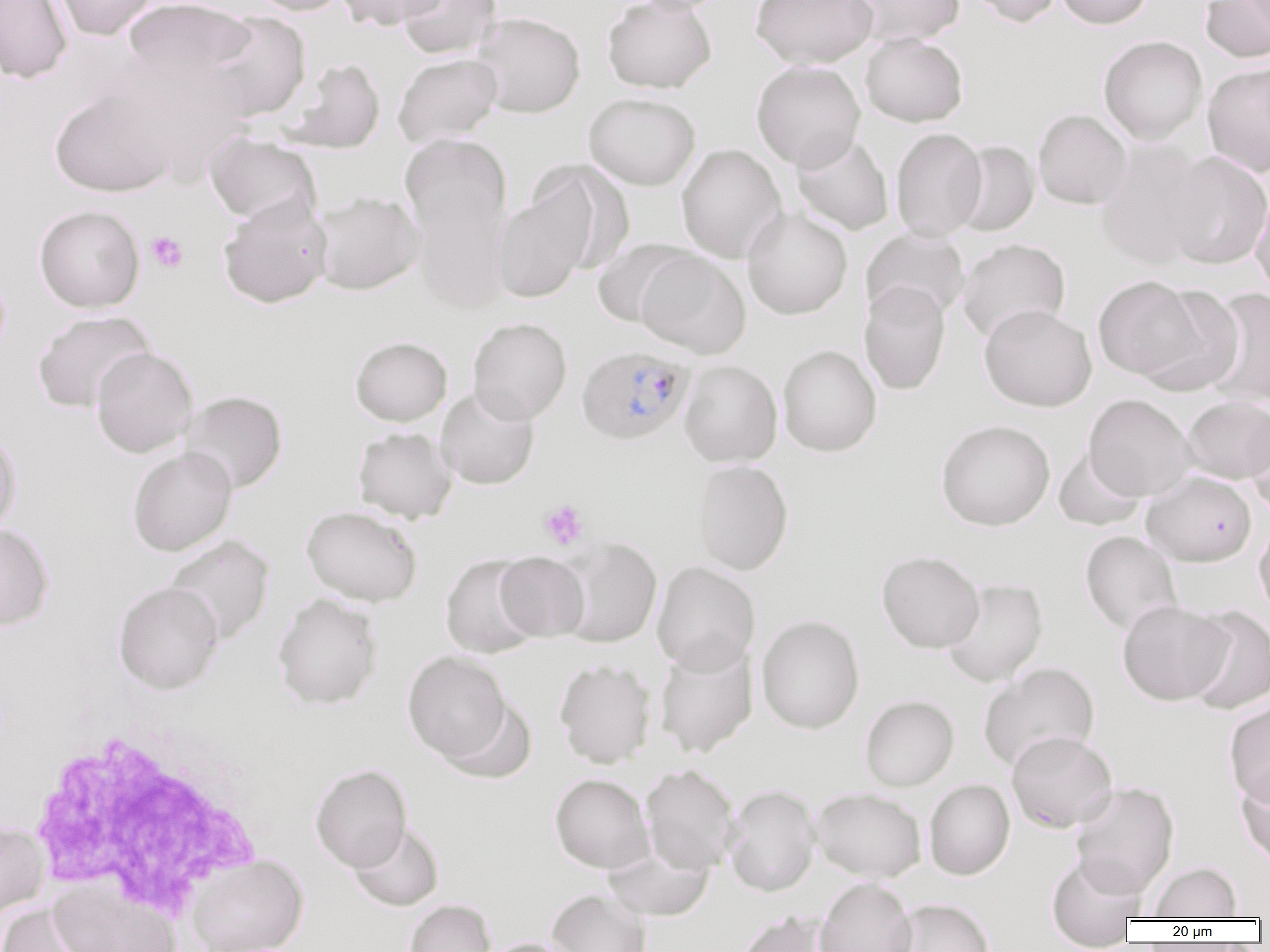
slide-level diagnosis = Plasmodium falciparum
field of view = one of a larger specimen
uninfected red blood cell locations = approximate bounding boxes as (x1, y1, x2, y2) in pixels: (0, 0, 73, 84), (50, 0, 159, 41), (123, 0, 255, 85), (245, 0, 351, 16), (335, 0, 446, 30), (396, 0, 502, 60), (602, 0, 717, 94), (623, 0, 735, 15), (751, 0, 878, 69), (846, 0, 965, 47), (964, 0, 1062, 27), (1055, 0, 1154, 29), (1200, 0, 1270, 62), (203, 11, 311, 121), (471, 12, 586, 118), (860, 33, 968, 127), (1098, 35, 1208, 145), (392, 53, 503, 147), (110, 54, 251, 182), (280, 57, 385, 154), (751, 60, 865, 171), (1202, 63, 1270, 176), (49, 87, 176, 198), (584, 92, 701, 190), (1033, 109, 1132, 209), (890, 127, 987, 241), (204, 132, 322, 226), (400, 132, 514, 286), (790, 132, 894, 235), (951, 141, 1039, 236), (1096, 141, 1215, 269), (676, 144, 787, 263), (1162, 152, 1270, 269), (527, 160, 634, 274), (1251, 187, 1270, 299), (491, 188, 593, 303), (311, 191, 423, 295), (218, 196, 333, 309), (34, 204, 145, 313), (742, 206, 853, 320), (860, 228, 970, 324), (956, 238, 1070, 343), (591, 239, 696, 328), (635, 250, 751, 358), (1092, 275, 1206, 381), (859, 282, 951, 395), (1135, 284, 1244, 396), (1200, 287, 1270, 407), (979, 304, 1097, 412), (32, 310, 155, 413), (467, 317, 572, 425), (349, 336, 452, 426), (777, 345, 882, 457), (91, 346, 198, 457), (679, 360, 783, 467), (436, 387, 540, 489), (179, 390, 288, 494), (1083, 393, 1197, 501), (1183, 396, 1270, 483), (1244, 406, 1270, 514), (935, 419, 1055, 531), (0, 425, 22, 536), (353, 426, 458, 524), (127, 446, 237, 556), (1053, 446, 1148, 531), (691, 459, 794, 575), (1141, 471, 1257, 567), (302, 505, 422, 607), (1254, 518, 1270, 626), (0, 523, 53, 631), (1080, 530, 1183, 636), (163, 535, 275, 646), (556, 537, 662, 648), (876, 550, 985, 653), (494, 552, 590, 641), (441, 554, 544, 659), (651, 561, 761, 675), (940, 578, 1047, 687), (113, 581, 224, 694), (272, 592, 383, 710), (1117, 600, 1233, 705), (1182, 606, 1270, 714), (756, 615, 865, 734), (654, 639, 758, 758), (402, 651, 511, 765), (554, 659, 656, 768), (977, 662, 1100, 772), (859, 694, 959, 791), (441, 696, 536, 784), (1224, 699, 1270, 807), (1006, 730, 1118, 833), (310, 764, 412, 872), (640, 764, 741, 874), (1236, 765, 1270, 868), (549, 773, 654, 873), (923, 778, 1015, 880), (1069, 781, 1179, 898), (722, 785, 821, 897), (811, 788, 927, 881), (0, 820, 49, 919), (347, 822, 444, 911), (602, 841, 714, 922), (1046, 853, 1147, 949), (186, 854, 309, 952), (1148, 861, 1242, 920), (814, 877, 917, 952), (49, 881, 180, 952), (546, 889, 651, 952), (890, 898, 996, 952), (404, 899, 496, 952), (0, 902, 103, 952), (735, 910, 839, 952), (480, 938, 581, 952)
white blood cell locations = approximate bounding boxes as (x1, y1, x2, y2) in pixels: (21, 715, 273, 916)
platelet locations = approximate bounding boxes as (x1, y1, x2, y2) in pixels: (146, 231, 188, 273), (538, 499, 589, 550)
Plasmodium falciparum-infected red blood cell locations = approximate bounding boxes as (x1, y1, x2, y2) in pixels: (576, 345, 696, 445)
image size = 1270×952 pixels
preparation = thin blood smear
modality = optical microscopy
magnification = 1000x